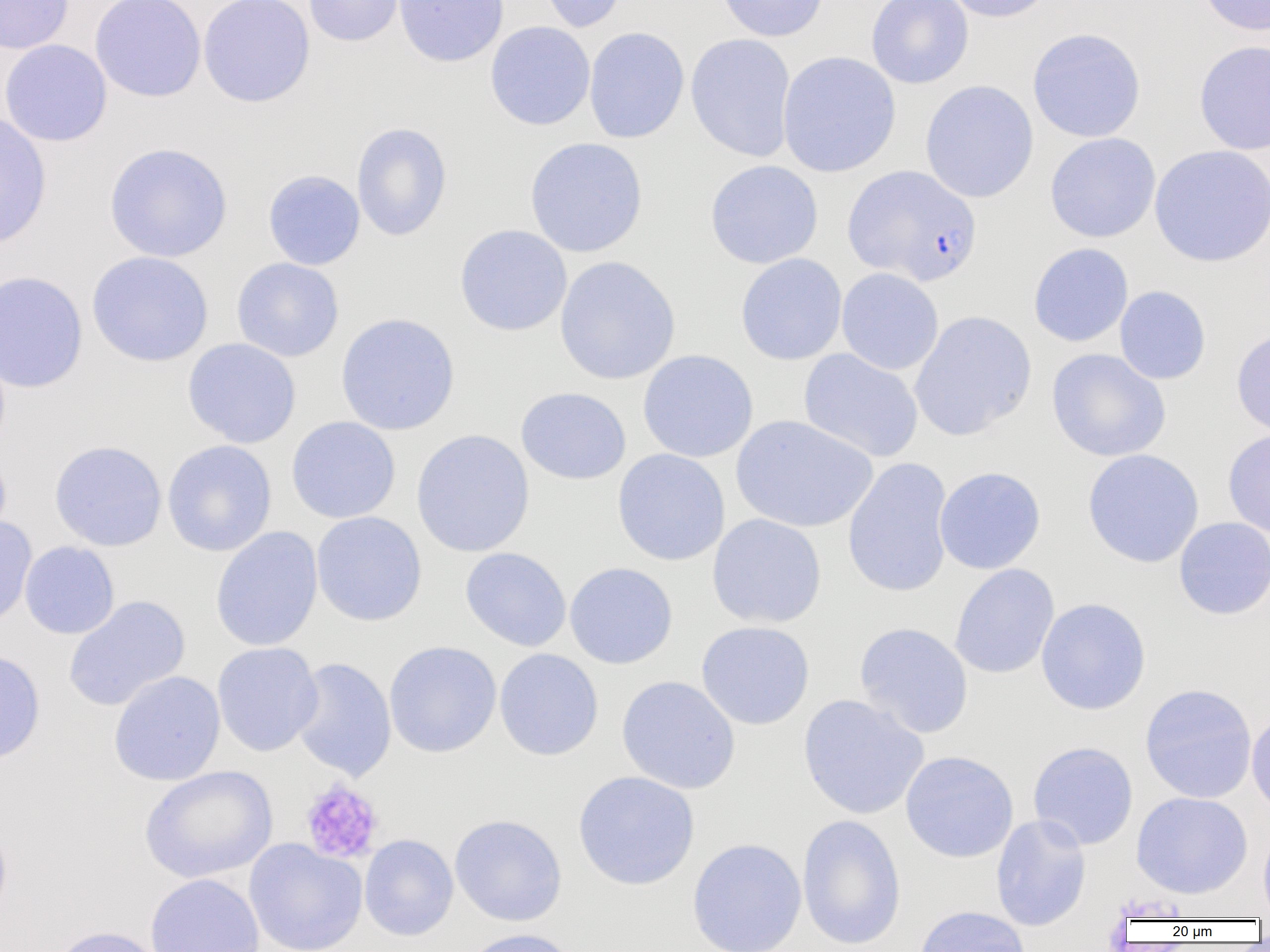 Approximate bounding boxes as named x1/y1/x2/y2 corners in pixels. Uninfected red blood cell locations: (x1=0, y1=0, x2=74, y2=54), (x1=89, y1=0, x2=207, y2=102), (x1=198, y1=0, x2=316, y2=107), (x1=302, y1=0, x2=405, y2=47), (x1=393, y1=0, x2=509, y2=67), (x1=535, y1=0, x2=629, y2=33), (x1=716, y1=0, x2=829, y2=42), (x1=866, y1=0, x2=973, y2=89), (x1=938, y1=0, x2=1057, y2=23), (x1=1196, y1=0, x2=1270, y2=36), (x1=485, y1=21, x2=596, y2=131), (x1=583, y1=27, x2=690, y2=143), (x1=1027, y1=28, x2=1146, y2=143), (x1=686, y1=33, x2=797, y2=162), (x1=0, y1=39, x2=112, y2=147), (x1=1194, y1=40, x2=1270, y2=156), (x1=777, y1=51, x2=901, y2=177), (x1=920, y1=80, x2=1039, y2=203), (x1=0, y1=112, x2=52, y2=250), (x1=351, y1=122, x2=453, y2=242), (x1=1045, y1=133, x2=1161, y2=243), (x1=524, y1=137, x2=649, y2=258), (x1=103, y1=142, x2=234, y2=263), (x1=1150, y1=145, x2=1270, y2=267), (x1=704, y1=160, x2=824, y2=269), (x1=263, y1=170, x2=365, y2=270), (x1=454, y1=224, x2=573, y2=336), (x1=1028, y1=242, x2=1134, y2=347), (x1=86, y1=251, x2=214, y2=367), (x1=735, y1=253, x2=848, y2=366), (x1=554, y1=256, x2=680, y2=385), (x1=232, y1=257, x2=344, y2=362), (x1=836, y1=267, x2=944, y2=375), (x1=0, y1=269, x2=88, y2=393), (x1=1114, y1=285, x2=1211, y2=385), (x1=909, y1=310, x2=1037, y2=441), (x1=335, y1=312, x2=460, y2=435), (x1=1231, y1=326, x2=1270, y2=439), (x1=182, y1=338, x2=301, y2=448), (x1=798, y1=348, x2=924, y2=463), (x1=1046, y1=348, x2=1171, y2=462), (x1=637, y1=349, x2=758, y2=463), (x1=515, y1=386, x2=631, y2=485), (x1=731, y1=415, x2=877, y2=533), (x1=286, y1=416, x2=401, y2=524), (x1=410, y1=429, x2=535, y2=557), (x1=1223, y1=429, x2=1270, y2=539), (x1=162, y1=439, x2=277, y2=557), (x1=49, y1=440, x2=167, y2=551), (x1=0, y1=448, x2=12, y2=550), (x1=612, y1=448, x2=730, y2=566), (x1=1082, y1=449, x2=1205, y2=568), (x1=842, y1=457, x2=955, y2=598), (x1=934, y1=466, x2=1046, y2=574), (x1=311, y1=511, x2=427, y2=627), (x1=707, y1=514, x2=827, y2=628), (x1=0, y1=516, x2=37, y2=630), (x1=1173, y1=517, x2=1270, y2=620), (x1=210, y1=526, x2=324, y2=652), (x1=20, y1=541, x2=120, y2=639), (x1=460, y1=547, x2=572, y2=652), (x1=564, y1=562, x2=679, y2=670), (x1=949, y1=563, x2=1060, y2=679), (x1=63, y1=595, x2=191, y2=711), (x1=1035, y1=597, x2=1152, y2=716), (x1=695, y1=620, x2=815, y2=730), (x1=854, y1=622, x2=974, y2=739), (x1=384, y1=641, x2=502, y2=758), (x1=212, y1=642, x2=323, y2=757), (x1=0, y1=648, x2=46, y2=766), (x1=494, y1=648, x2=604, y2=761), (x1=289, y1=657, x2=397, y2=781), (x1=108, y1=670, x2=225, y2=786), (x1=616, y1=675, x2=741, y2=794), (x1=1139, y1=683, x2=1257, y2=804), (x1=797, y1=693, x2=929, y2=820), (x1=1246, y1=707, x2=1270, y2=819), (x1=1027, y1=741, x2=1139, y2=850), (x1=900, y1=750, x2=1019, y2=863), (x1=139, y1=765, x2=278, y2=883), (x1=573, y1=770, x2=700, y2=891), (x1=1131, y1=791, x2=1253, y2=899), (x1=449, y1=814, x2=567, y2=927), (x1=797, y1=814, x2=907, y2=951), (x1=990, y1=814, x2=1091, y2=932), (x1=0, y1=821, x2=13, y2=928), (x1=1258, y1=822, x2=1270, y2=920), (x1=359, y1=834, x2=459, y2=941), (x1=686, y1=837, x2=808, y2=952), (x1=244, y1=839, x2=367, y2=952), (x1=144, y1=873, x2=265, y2=952), (x1=913, y1=905, x2=1030, y2=952), (x1=49, y1=925, x2=168, y2=952), (x1=460, y1=927, x2=580, y2=952). Platelet locations: (x1=299, y1=779, x2=385, y2=865). Plasmodium falciparum-infected red blood cell locations: (x1=843, y1=165, x2=982, y2=287). Slide-level diagnosis: Plasmodium falciparum. Single field of view. Thin blood smear. Image is 1270×952 pixels. Light microscopy. 1000x magnification.